Report the malaria status of this cell.
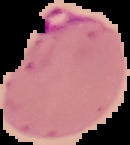

It is parasitized.

{
  "image_size": "130×145 pixels",
  "preparation": "thin blood smear",
  "image_type": "cell region segmented out of the field of view; surrounding area masked to black"
}